Report the malaria status.
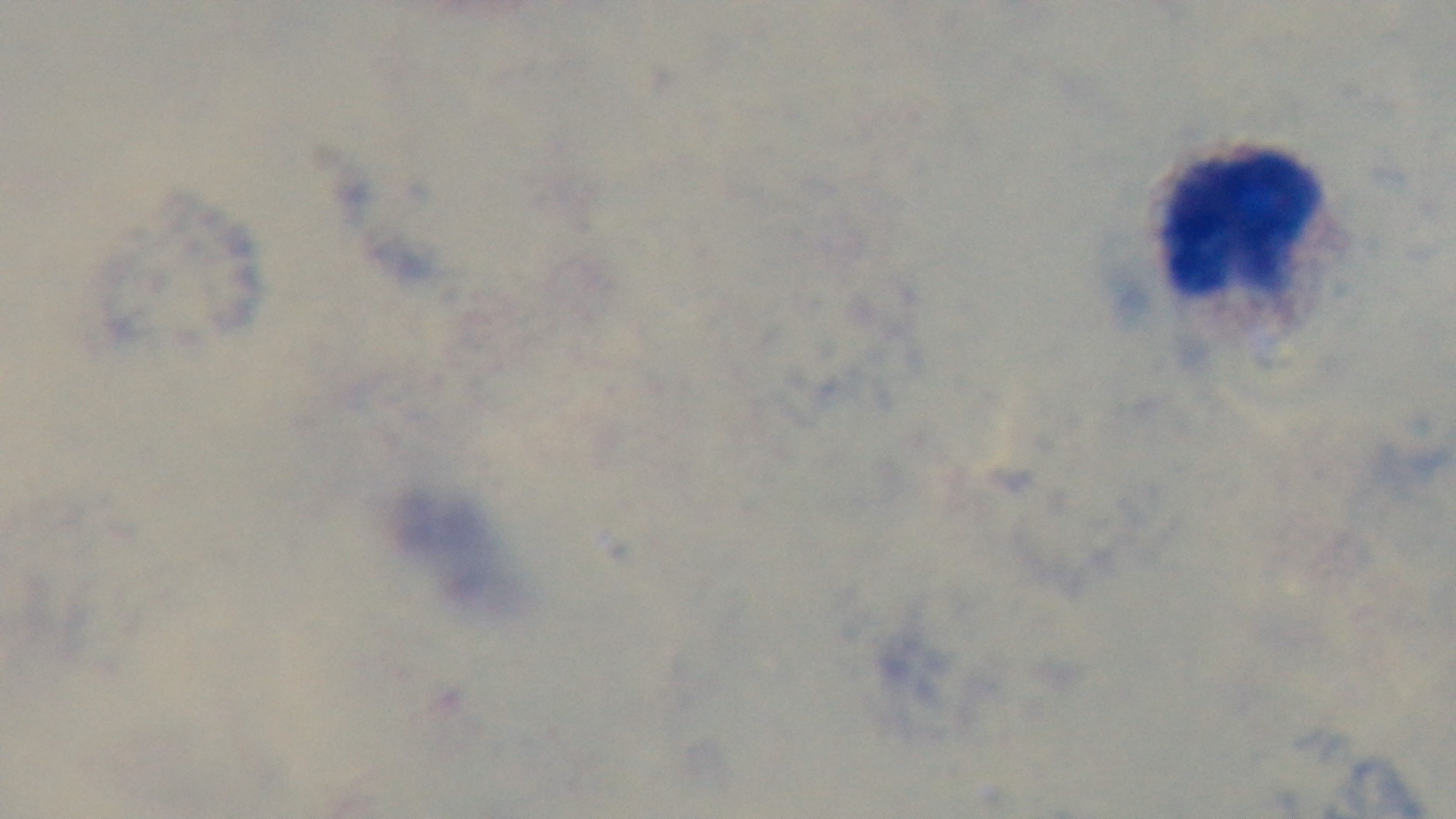
Uninfected.

Mounted 4K digital camera. Photomicrograph. Preparation: thick smear. One field from the slide. Oil-immersion objective, 100x. Giemsa-stained.